Assess this cell for malaria.
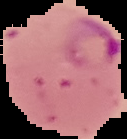
Parasitized.

Summary:
  - Preparation: thin blood smear
  - Image size: 127×139 pixels
  - Image type: segmented cell region on a black background